Outline each blood parasite and name the species.
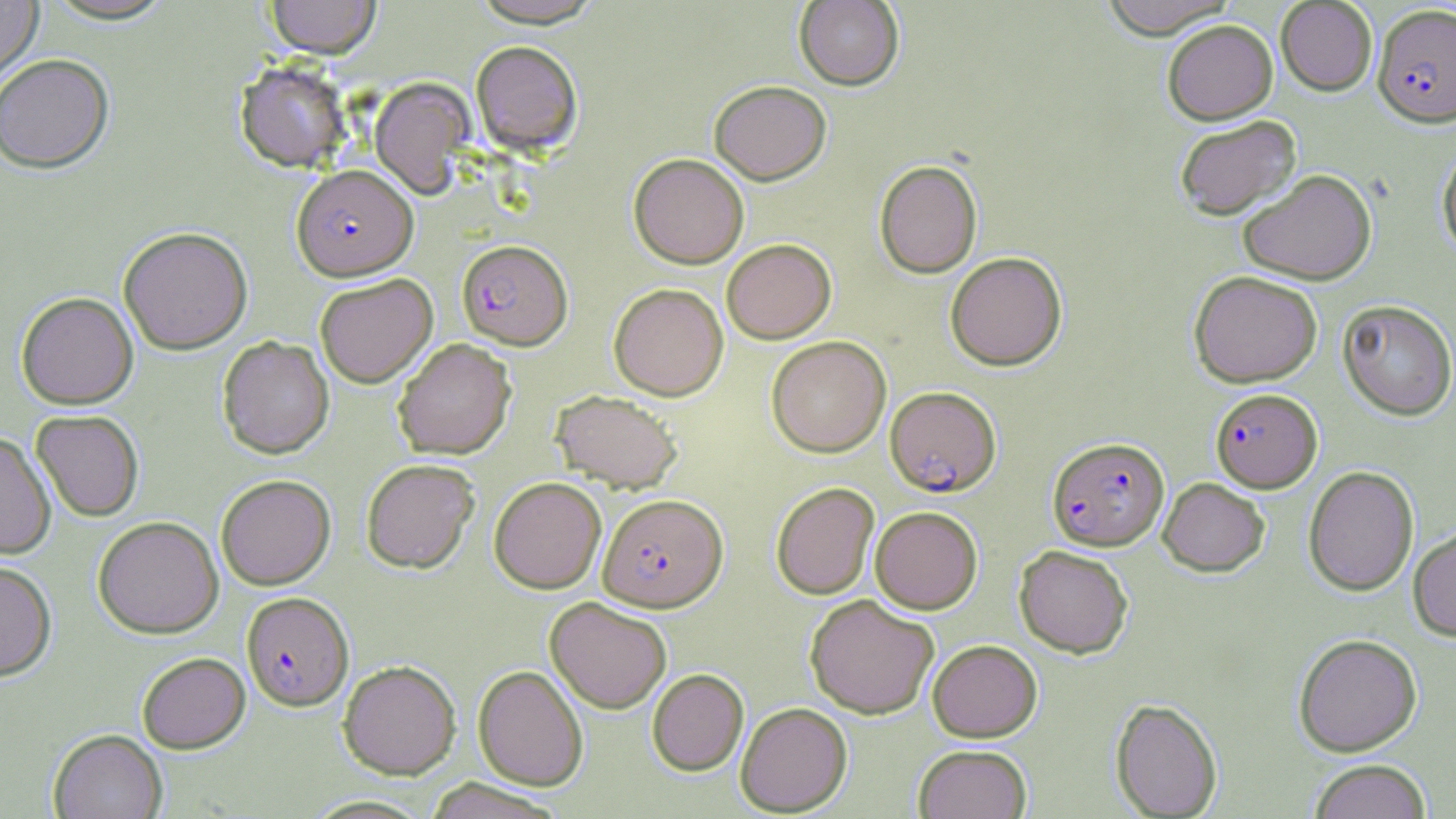
Approximate bounding boxes as (x1, y1, x2, y2) in pixels.
Plasmodium falciparum-infected red blood cells: (1373, 4, 1456, 128), (291, 165, 418, 280), (457, 239, 572, 349), (885, 386, 1001, 497), (1210, 388, 1322, 492), (1047, 437, 1169, 550), (598, 493, 728, 612), (241, 592, 353, 711).
No Plasmodium ovale, Plasmodium malariae, Plasmodium vivax, Babesia divergens, or Trypanosoma brucei observed.

Uninfected red blood cell locations: (0, 0, 43, 83), (41, 0, 179, 26), (265, 0, 381, 60), (794, 0, 904, 91), (1097, 0, 1238, 39), (1276, 1, 1377, 95), (1162, 20, 1278, 124), (470, 40, 583, 156), (0, 54, 114, 174), (234, 61, 353, 173), (369, 78, 476, 199), (709, 80, 831, 185), (1173, 115, 1301, 221), (1436, 142, 1456, 259), (629, 154, 749, 269), (874, 160, 983, 279), (1238, 168, 1377, 285), (118, 226, 253, 355), (721, 239, 836, 344), (945, 251, 1067, 371), (1188, 270, 1322, 387), (314, 274, 438, 388), (608, 283, 728, 401), (16, 292, 138, 410), (1337, 299, 1456, 420), (217, 335, 334, 460), (766, 335, 891, 458), (392, 338, 516, 460), (551, 390, 682, 492), (31, 410, 144, 522), (0, 432, 56, 560), (361, 458, 480, 574), (1303, 465, 1419, 596), (216, 474, 336, 590), (489, 476, 606, 594), (1158, 477, 1270, 576), (770, 482, 879, 600), (870, 506, 983, 614), (93, 516, 224, 638), (1408, 525, 1456, 641), (1014, 545, 1134, 658), (0, 561, 57, 682), (805, 594, 940, 719), (545, 597, 672, 713), (1293, 633, 1422, 756), (927, 639, 1042, 742), (137, 652, 250, 753), (338, 660, 461, 779), (473, 665, 588, 790), (647, 668, 748, 776), (1110, 698, 1223, 818), (736, 702, 852, 816), (48, 728, 167, 819), (913, 744, 1032, 819), (1308, 759, 1432, 819), (421, 779, 567, 819), (300, 795, 437, 818). Slide-level diagnosis: Plasmodium falciparum. One field of a larger specimen. Captured at 1000x magnification. Optical microscopy. May-Grünwald-Giemsa-stained preparation. Thin blood smear. Image is 1456×819 pixels.